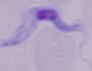

Photomicrograph. A trypanosome is seen. Captured at 1000x magnification.